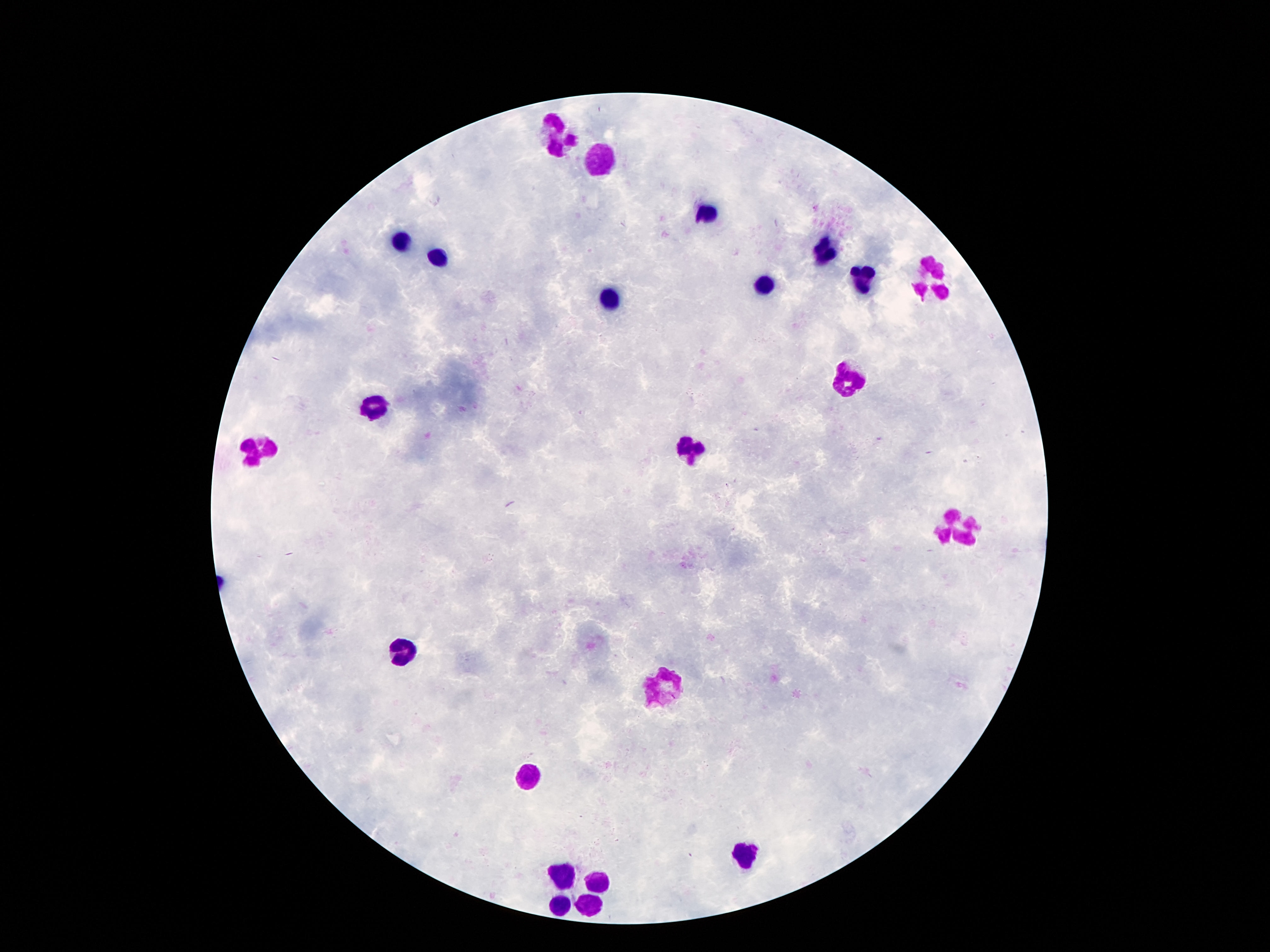

Approximate centers as (x, y) in pixels.
Summary:
  - Leukocyte locations: (561, 133), (603, 161), (704, 216), (400, 239), (823, 251), (440, 257), (932, 280), (860, 281), (767, 286), (610, 300), (849, 380), (377, 403), (690, 447), (256, 448), (958, 526), (400, 651), (659, 686), (527, 778), (744, 856), (566, 878), (594, 881), (585, 902), (559, 906)
  - Preparation: thick peripheral-blood smear
  - Stain: Giemsa
  - Image size: 1270×952 pixels
  - Magnification: 100x
  - Patient malaria status: negative
  - Field of view: one from this slide
  - Capture: smartphone camera through the microscope eyepiece